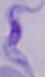

Summary:
  - Modality: micrograph
  - Magnification: 1000x
  - Identification: trypanosome